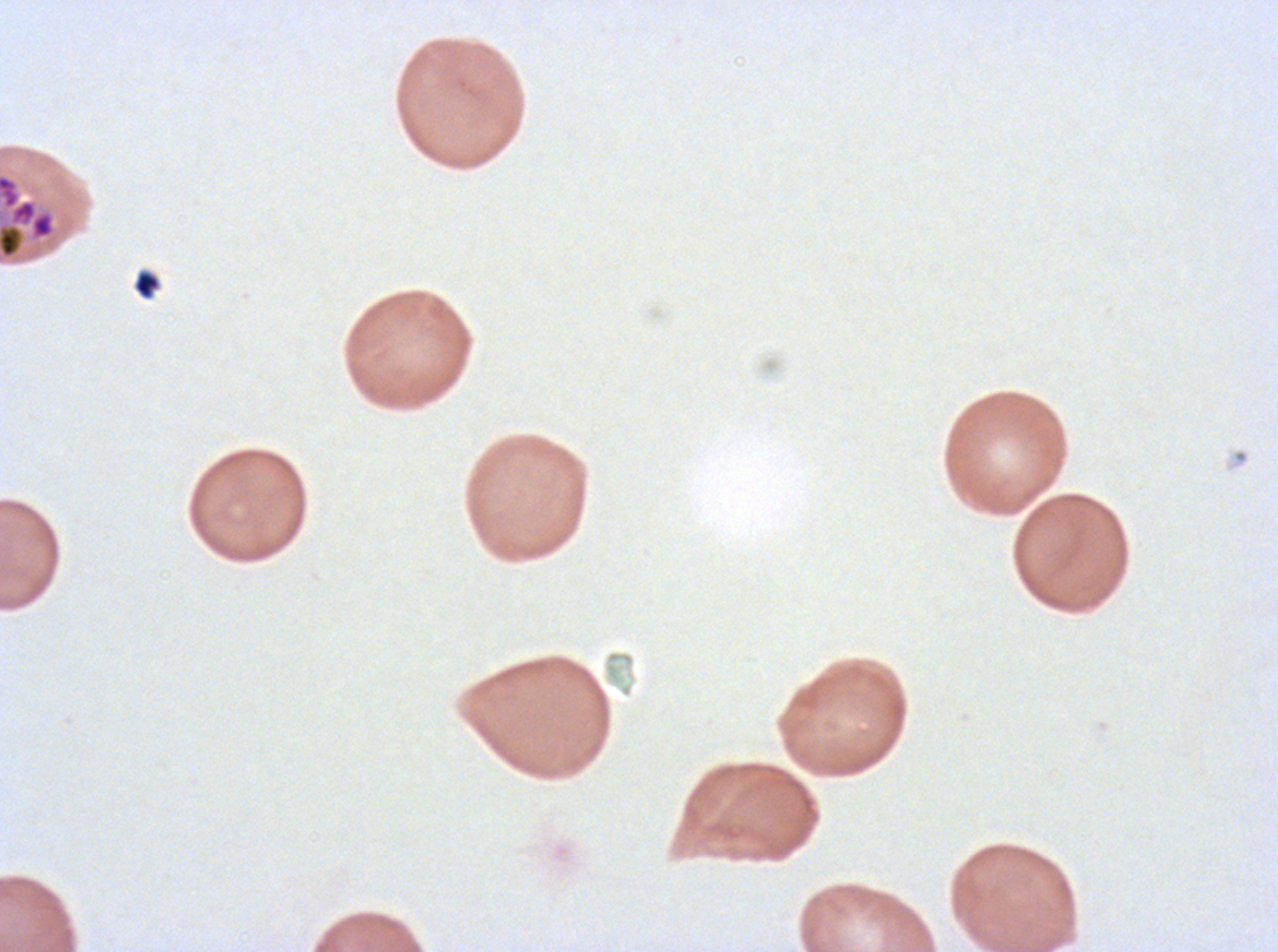

notation = approximate bounding boxes as {x1, y1, x2, y2} in pixels
late schizont locations = {0, 172, 57, 262}
debris locations = {132, 269, 161, 300}
image size = 1278×952 pixels
stain = Giemsa
field of view = sub-image separated from a larger composite
preparation = thin blood film
specimen = P. falciparum cultured ex vivo for 24 to 48 hours, from a patient in The Gambia